Report the malaria status of this cell.
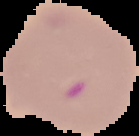
It is parasitized.

Image is 139×136 pixels. From a thin blood film. Segmented cell region on a black background.